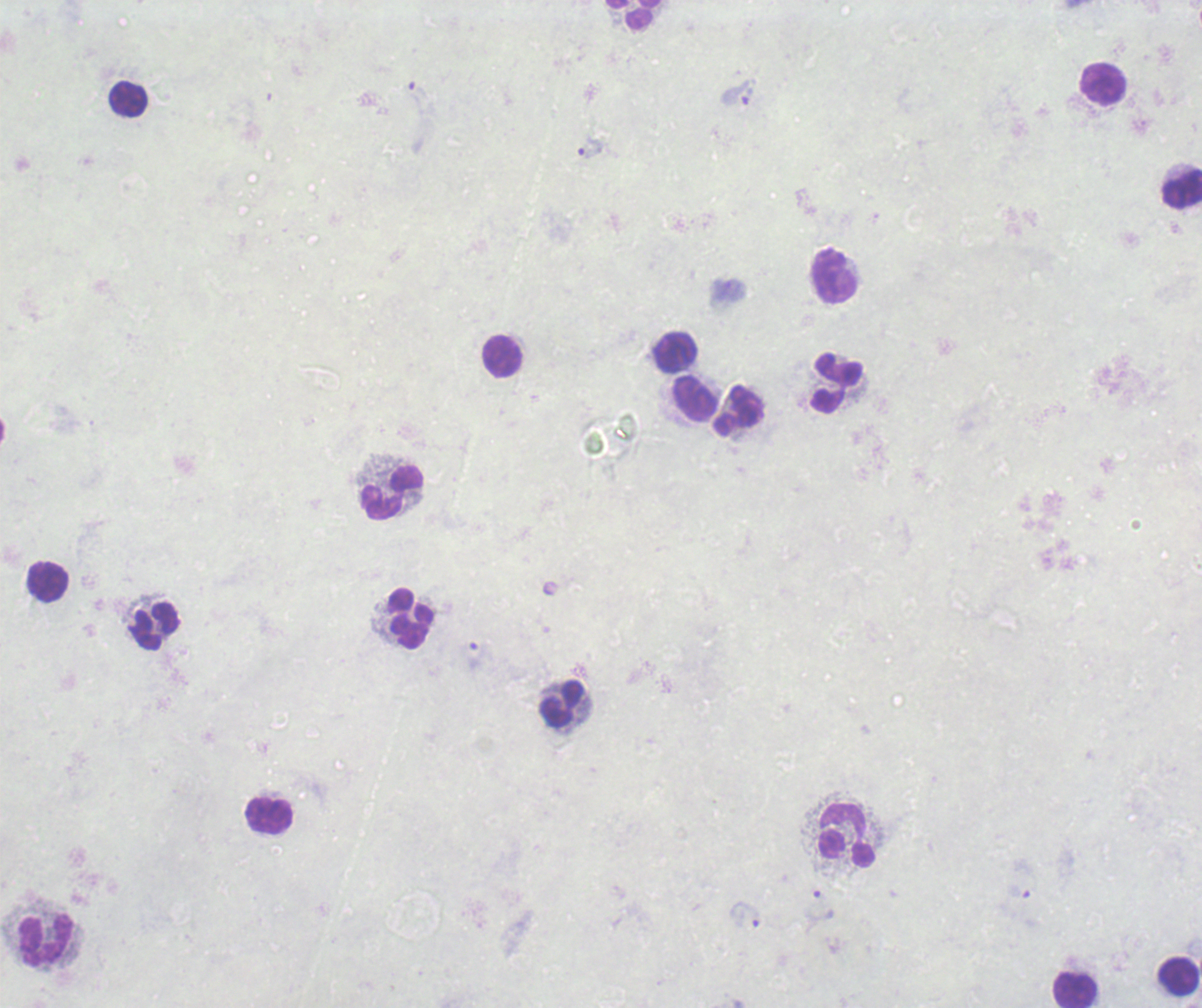
coordinate format = approximate centers as (x, y) in pixels
trophozoite locations = (736, 92), (589, 149), (745, 914)
leukocyte locations = (633, 14), (1102, 84), (127, 97), (1182, 188), (834, 277), (675, 352), (502, 358), (836, 382), (695, 399), (739, 410), (391, 491), (48, 582), (411, 618), (154, 627), (562, 704), (269, 817), (846, 838), (47, 941), (1178, 977), (1074, 989)
image size = 1202×1008 pixels
context = previously used in a real diagnosis
field of view = one from this slide
result = positive for Plasmodium parasites
background quality = unsatisfactory
stain = Romanowsky
magnification = 100x
preparation = thick smear of blood